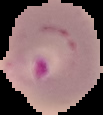

Summary:
  - Preparation: thin blood smear
  - Image type: cell region segmented out of the field of view; surrounding area masked to black
  - Malaria status: parasitized
  - Image size: 103×115 pixels